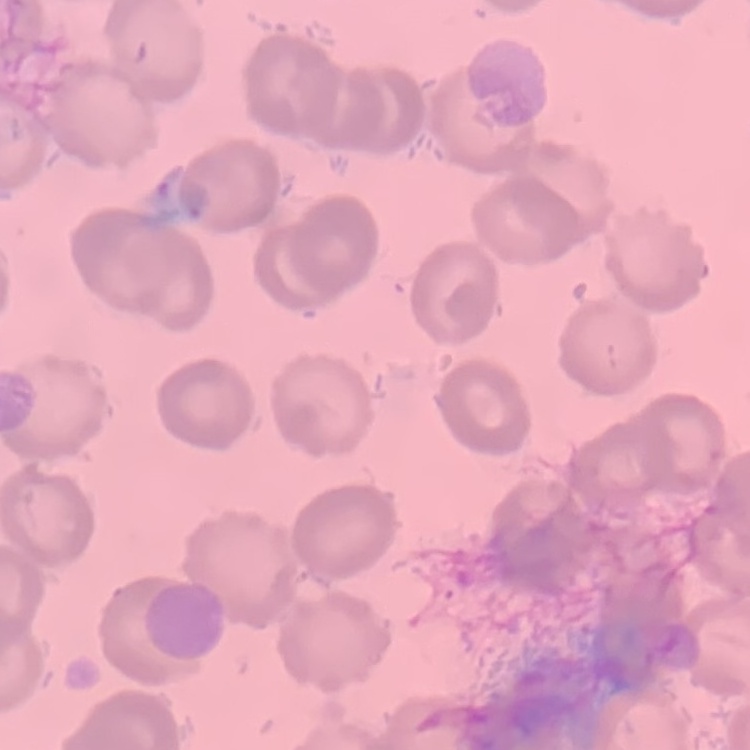
erythrocyte morphology = no rouleaux formation
image type = square crop of a larger photomicrograph
preparation = thin peripheral smear
stain = Field's or Giemsa